Identify the preparation type.
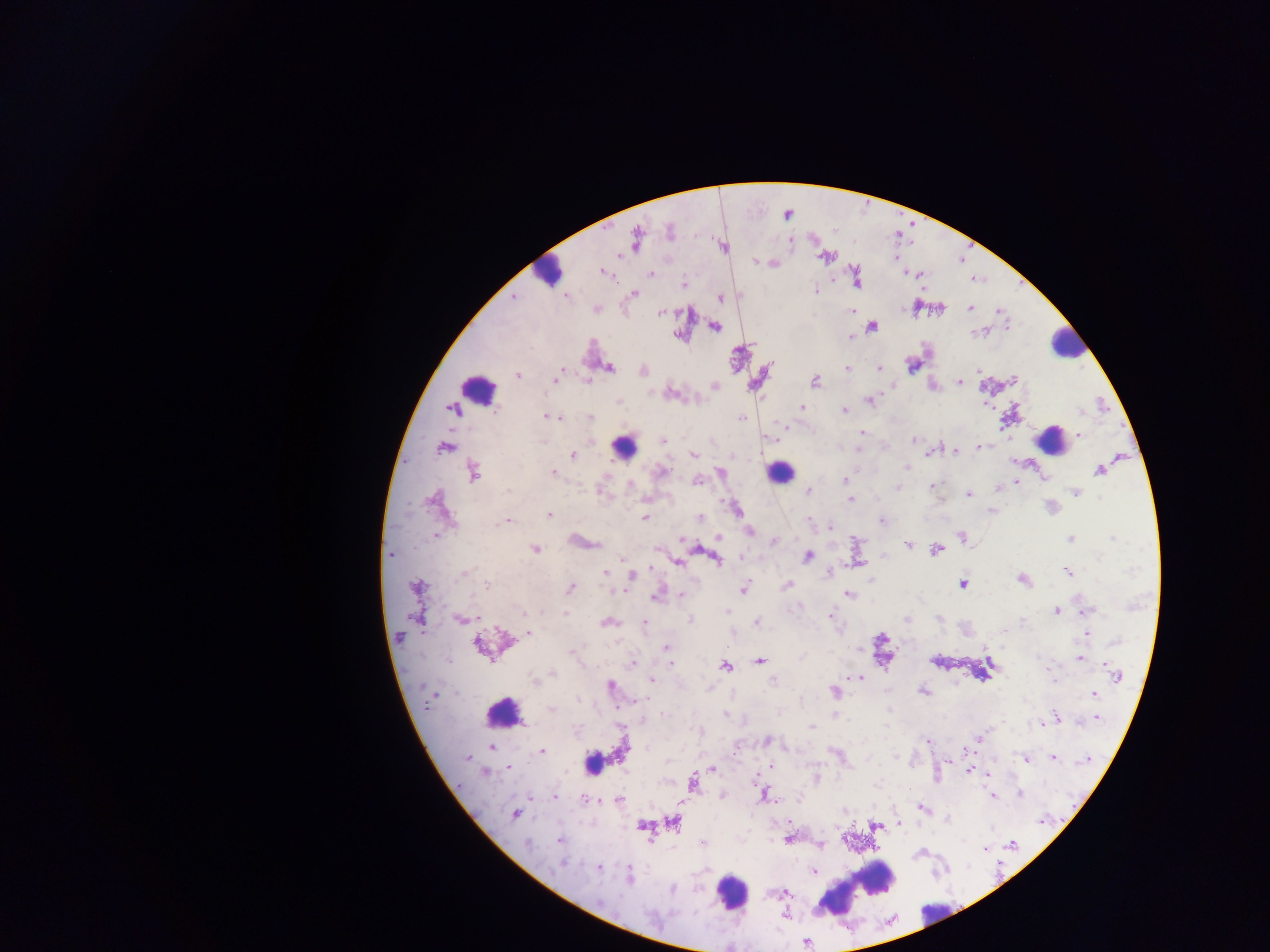

Thick blood smear.

Approximate centers as [x, y] in pixels. Leukocyte locations (subset; some below the resolvable size): [551, 265], [1067, 345], [477, 389], [1049, 440], [626, 447], [779, 472], [504, 714], [592, 762], [867, 884], [731, 893], [832, 901], [934, 911]. Plasmodium parasite locations: [670, 232], [636, 240], [621, 254], [824, 256], [895, 258], [755, 261], [603, 271], [650, 274], [683, 285], [815, 290], [634, 294], [514, 297], [566, 297], [720, 298], [941, 308], [970, 308], [596, 309], [851, 310], [998, 310], [661, 312], [715, 326], [872, 327], [851, 335], [912, 365], [609, 367], [847, 368], [879, 368], [979, 369], [561, 371], [643, 371], [518, 374], [1013, 378], [556, 379], [586, 381], [959, 381], [815, 382], [714, 386], [671, 394], [619, 401], [869, 401], [802, 407], [454, 409], [845, 411], [548, 417], [742, 417], [557, 418], [591, 418], [861, 433], [1079, 435], [914, 440], [663, 441], [917, 443], [980, 447], [444, 448], [858, 450], [954, 451], [929, 454], [693, 455], [573, 456], [906, 467], [662, 471], [1099, 471], [720, 472], [473, 473], [552, 473], [1044, 478], [845, 480], [697, 481], [1016, 482], [630, 486], [931, 486], [898, 487], [998, 488], [808, 491], [601, 492], [1076, 493], [969, 494], [1100, 497], [851, 499], [735, 508], [991, 510], [549, 514], [645, 517], [700, 518], [882, 521], [507, 522], [809, 522], [830, 526], [749, 531], [435, 536], [718, 536], [962, 537], [1112, 538], [1070, 539], [683, 540], [774, 541], [907, 544], [535, 548], [936, 549], [656, 550], [391, 555], [807, 557], [1100, 557], [742, 558], [622, 559], [717, 559], [678, 562], [650, 568], [1066, 571], [606, 572], [465, 573], [828, 573], [632, 576], [1022, 579], [870, 581], [963, 584], [787, 585], [487, 586], [417, 587], [569, 588], [744, 588], [848, 594], [681, 595], [656, 596], [1057, 611], [1086, 611], [523, 612], [565, 612], [727, 612], [830, 616], [460, 619], [938, 619], [418, 620], [690, 620], [907, 620], [1023, 620], [607, 622], [756, 622], [645, 623], [529, 632], [1086, 634], [1116, 642], [479, 645], [666, 648], [572, 652], [668, 653], [1038, 657], [1080, 658], [760, 661], [632, 664], [671, 664], [726, 666], [552, 674], [1116, 675], [651, 679], [860, 679], [1052, 681], [534, 682], [774, 682], [610, 686], [709, 688], [834, 691], [923, 691], [1094, 693], [577, 699], [642, 700], [551, 709], [725, 714], [665, 715], [1056, 716], [1097, 718], [1041, 723], [812, 727], [979, 736], [766, 740], [927, 740], [491, 747], [542, 751], [835, 753], [1053, 758], [467, 759], [1026, 760], [1085, 761], [771, 766], [508, 768], [713, 769], [969, 771], [486, 772], [988, 774], [694, 783], [1020, 793], [764, 795], [993, 795], [722, 796], [554, 797], [584, 799], [619, 800], [681, 802], [920, 808], [514, 815], [947, 820], [1042, 821], [673, 822], [790, 822], [899, 823], [643, 826], [875, 826], [559, 840], [788, 840], [702, 842], [527, 844], [821, 845], [1013, 845], [985, 848], [562, 864], [598, 867], [814, 871], [630, 875], [788, 893], [600, 904], [806, 943]. Mobile-phone photograph taken through the microscope. Image is 1270×952 pixels. Single field of view. Sample from Ghana.